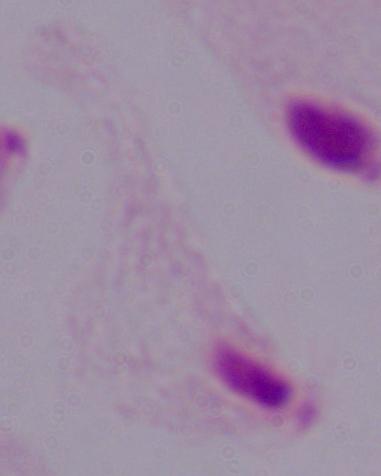
magnification: 1000x
identification: trichomonad
modality: micrograph